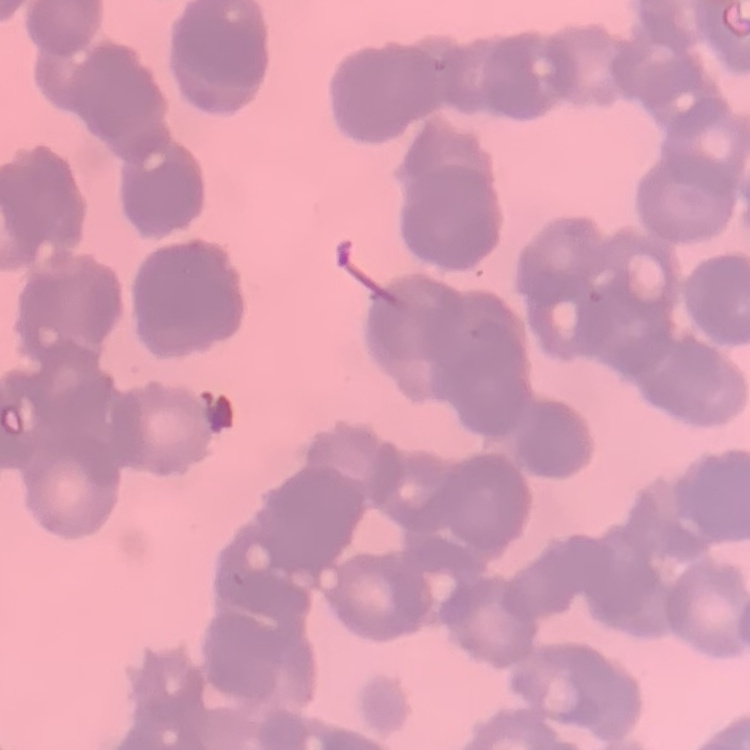 The erythrocytes show rouleaux formation. One tile cut from a larger photomicrograph. Stained with either Field's or Giemsa. Thin blood film.